Report the malaria status.
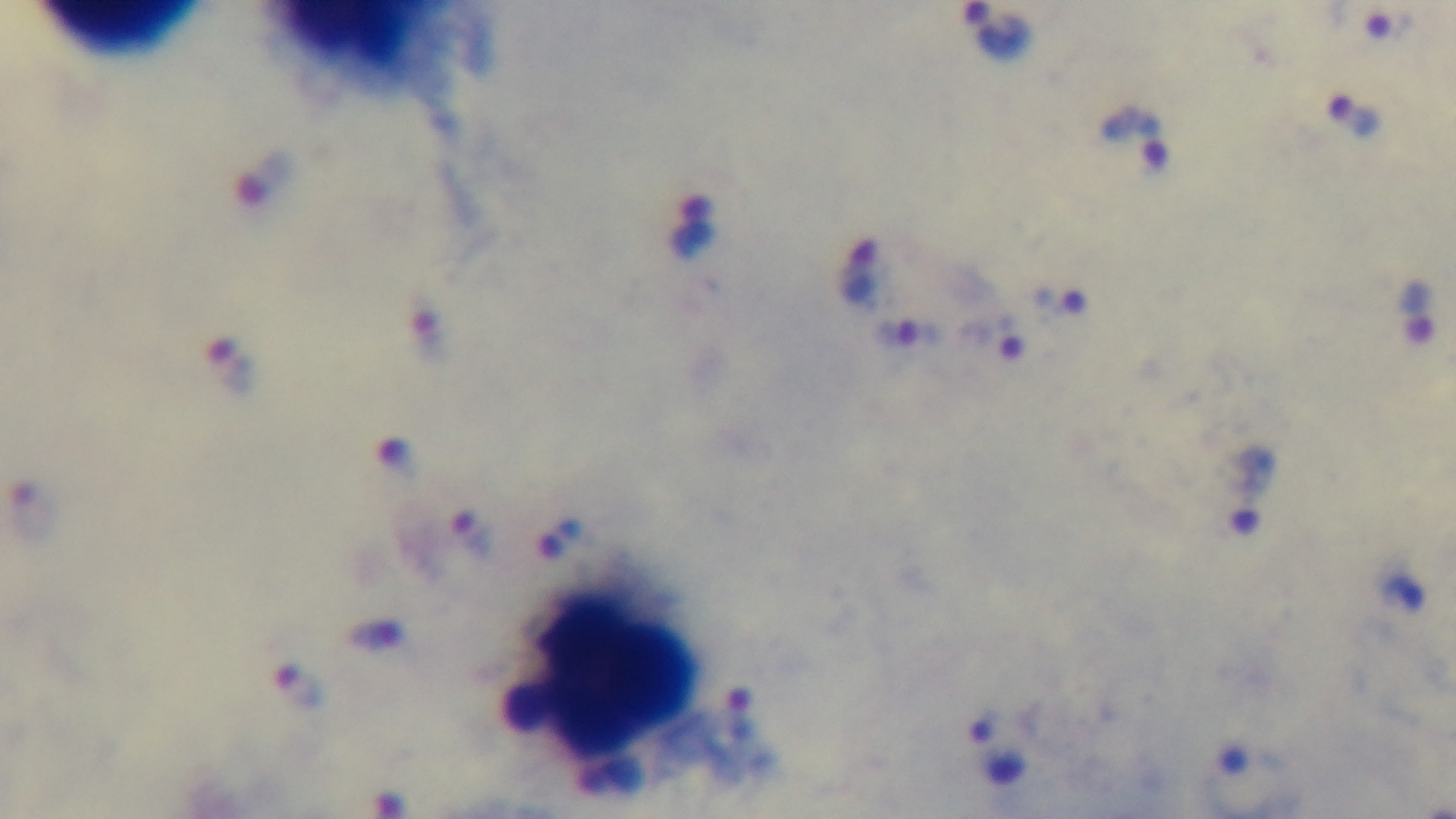

It is infected.

Captured with a mounted 4K digital camera. Single field of view. Giemsa stain. 100x oil-immersion objective. Photomicrograph. Preparation: thick.